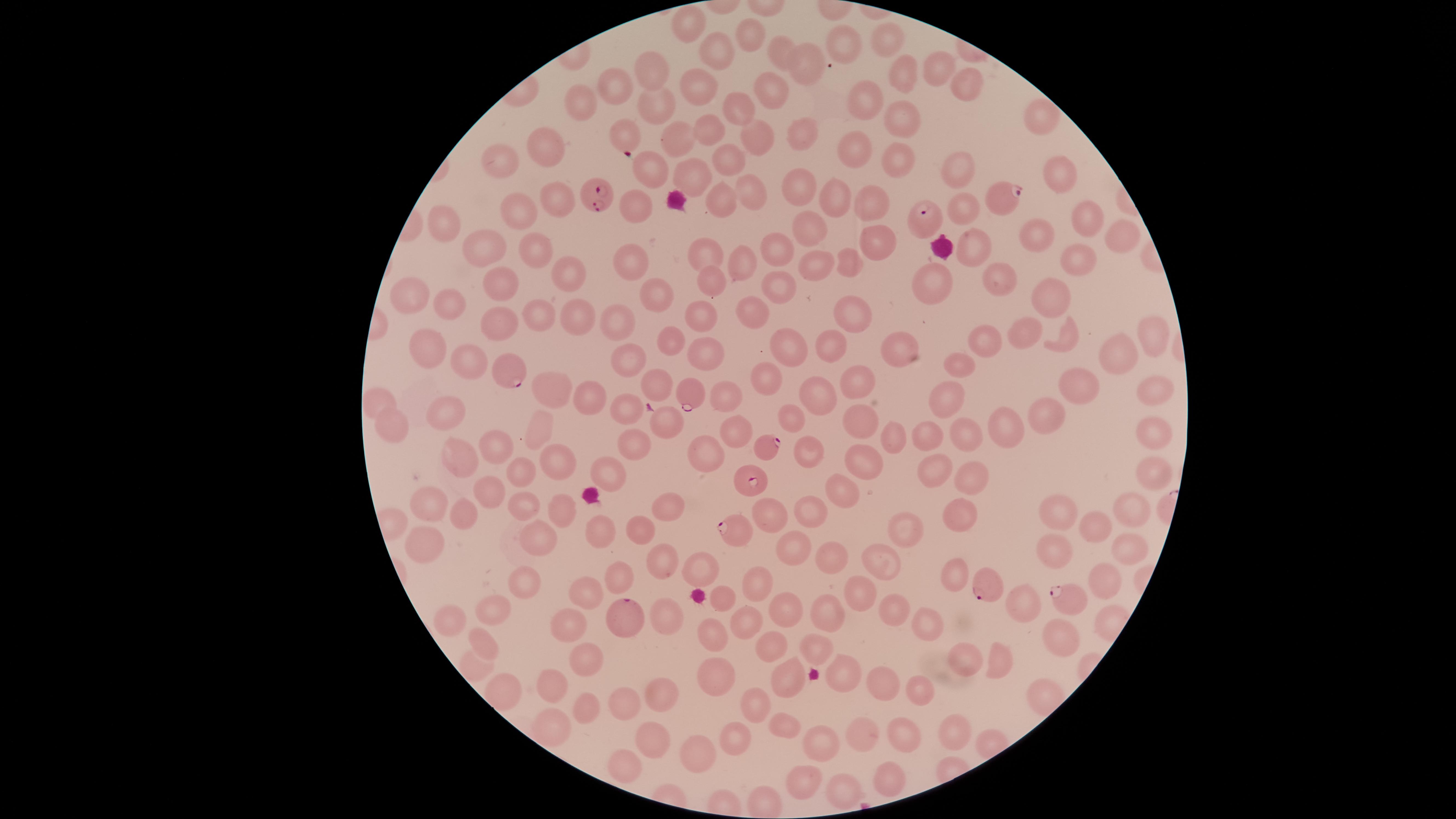
Approximate marker points, in pixels from the top-left corner.
Summary:
  - Parasitized red blood cells: (x=624, y=133), (x=599, y=197), (x=1007, y=197), (x=926, y=221), (x=514, y=374), (x=692, y=390), (x=768, y=451), (x=755, y=483), (x=740, y=531), (x=986, y=583), (x=1069, y=598), (x=624, y=614)
  - Uninfected red blood cells: (x=692, y=22), (x=750, y=37), (x=889, y=40), (x=844, y=44), (x=784, y=55), (x=716, y=56), (x=812, y=64), (x=937, y=68), (x=650, y=70), (x=903, y=70), (x=618, y=85), (x=967, y=86), (x=768, y=91), (x=699, y=95), (x=859, y=101), (x=655, y=106), (x=584, y=107), (x=736, y=113), (x=894, y=115), (x=1041, y=115), (x=706, y=131), (x=674, y=136), (x=797, y=138), (x=755, y=140), (x=855, y=151), (x=544, y=152), (x=727, y=161), (x=504, y=164), (x=899, y=165), (x=647, y=171), (x=955, y=173), (x=1060, y=174), (x=689, y=177), (x=800, y=184), (x=750, y=192), (x=837, y=196), (x=554, y=197), (x=871, y=199), (x=719, y=202), (x=527, y=208), (x=637, y=208), (x=966, y=209), (x=1082, y=216), (x=446, y=223), (x=813, y=228), (x=1120, y=232), (x=874, y=241), (x=1035, y=241), (x=971, y=247), (x=481, y=248), (x=535, y=248), (x=705, y=249), (x=775, y=250), (x=744, y=260), (x=816, y=262), (x=1080, y=262), (x=849, y=264), (x=628, y=266), (x=564, y=272), (x=933, y=275), (x=706, y=280), (x=995, y=280), (x=500, y=283), (x=778, y=284), (x=416, y=295), (x=1053, y=296), (x=651, y=299), (x=453, y=306), (x=749, y=315), (x=702, y=316), (x=848, y=316), (x=538, y=318), (x=577, y=318), (x=502, y=319), (x=621, y=321), (x=1030, y=334), (x=1147, y=337), (x=1067, y=341), (x=989, y=342), (x=790, y=343), (x=677, y=347), (x=833, y=347), (x=426, y=348), (x=897, y=354), (x=626, y=355), (x=1117, y=355), (x=705, y=359), (x=962, y=363), (x=468, y=368), (x=766, y=375), (x=858, y=377), (x=1075, y=384), (x=548, y=386), (x=1152, y=389), (x=657, y=391), (x=819, y=392), (x=586, y=398), (x=722, y=398), (x=951, y=398), (x=380, y=403), (x=630, y=407), (x=1045, y=412), (x=451, y=416), (x=856, y=419), (x=788, y=421), (x=1003, y=421), (x=669, y=425), (x=389, y=427), (x=738, y=430), (x=1156, y=433), (x=541, y=435), (x=927, y=435), (x=966, y=435), (x=898, y=438), (x=631, y=442), (x=495, y=447), (x=455, y=452), (x=806, y=453), (x=702, y=454), (x=864, y=460), (x=559, y=464), (x=521, y=469), (x=935, y=469), (x=611, y=472), (x=1147, y=476), (x=966, y=481), (x=840, y=489), (x=487, y=493), (x=667, y=503), (x=521, y=507), (x=1060, y=508), (x=810, y=509), (x=427, y=511), (x=1127, y=511), (x=563, y=514), (x=774, y=514), (x=461, y=516), (x=958, y=517), (x=1100, y=524), (x=908, y=529), (x=643, y=532), (x=605, y=536), (x=535, y=540), (x=427, y=545), (x=795, y=547), (x=1051, y=550), (x=1128, y=551), (x=662, y=553), (x=823, y=558), (x=708, y=561), (x=883, y=565), (x=956, y=574), (x=618, y=576), (x=526, y=580), (x=1103, y=585), (x=758, y=588), (x=587, y=592), (x=864, y=596), (x=725, y=598), (x=1024, y=605), (x=894, y=609), (x=495, y=610), (x=789, y=613), (x=450, y=619), (x=663, y=619), (x=829, y=619), (x=748, y=624), (x=569, y=625), (x=924, y=626), (x=1057, y=634), (x=716, y=637), (x=481, y=642), (x=768, y=643), (x=808, y=646), (x=960, y=657), (x=589, y=658), (x=844, y=667), (x=995, y=667), (x=472, y=668), (x=716, y=679), (x=553, y=680), (x=787, y=682), (x=883, y=686), (x=501, y=688), (x=917, y=690), (x=667, y=697), (x=624, y=702), (x=583, y=706), (x=756, y=707), (x=557, y=726), (x=787, y=728), (x=956, y=731), (x=858, y=732), (x=738, y=735), (x=906, y=736), (x=655, y=739), (x=822, y=744), (x=696, y=750), (x=625, y=769), (x=883, y=776), (x=801, y=780), (x=846, y=792)
  - Field of view: single
  - Presence: malaria parasites detected
  - Species: Plasmodium falciparum
  - Preparation: thin smear of blood
  - Visible region: circular
  - Capture: smartphone photograph through the microscope eyepiece
  - Stain: Giemsa
  - Image size: 1456×819 pixels